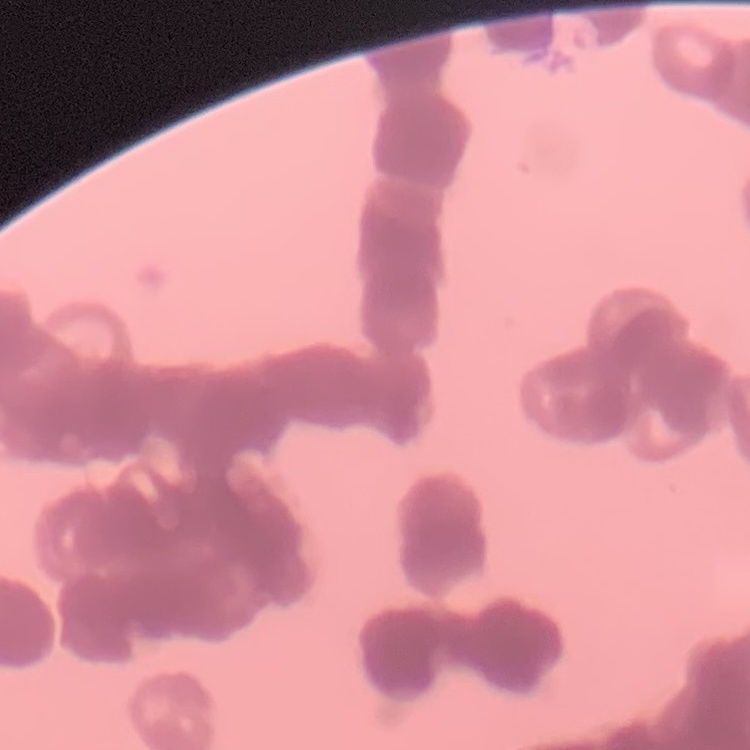
red blood cell morphology = rouleaux formation
preparation = thin blood smear
image type = one tile cut from a larger photomicrograph
stain = Field's or Giemsa